Assess this cell for malaria.
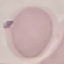
It is uninfected.

{
  "stain": "Giemsa",
  "capture": "smartphone camera at the microscope eyepiece",
  "preparation": "thin blood smear",
  "image_type": "cell patch, automatically extracted from a larger field of view and resized to 64 × 64 pixels"
}